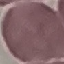

Result: negative for malaria parasites. Thin blood smear. Cell patch, automatically extracted from a larger field of view and resized to 64 × 64 pixels. Giemsa-stained preparation. Photographed with a smartphone camera at the microscope eyepiece.